Identify the parasite.
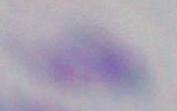

This is Toxoplasma gondii.

Captured at 1000x magnification. Photomicrograph.